State which parasite is depicted.
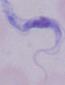

A trypanosome.

modality = photomicrograph
magnification = 1000x